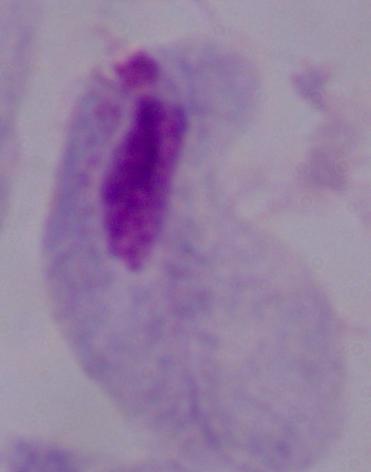 Captured at 1000x magnification. Photomicrograph. A trichomonad is seen.